Identify the cell.
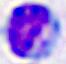
A leukocyte.

Photomicrograph. 400x magnification.